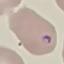

Result: malaria parasites identified. Thin smear of blood. Automatically extracted cell patch, resized to 64 × 64 pixels. Giemsa stain. Photographed with a smartphone camera at the microscope eyepiece.